Outline each blood parasite and name the species.
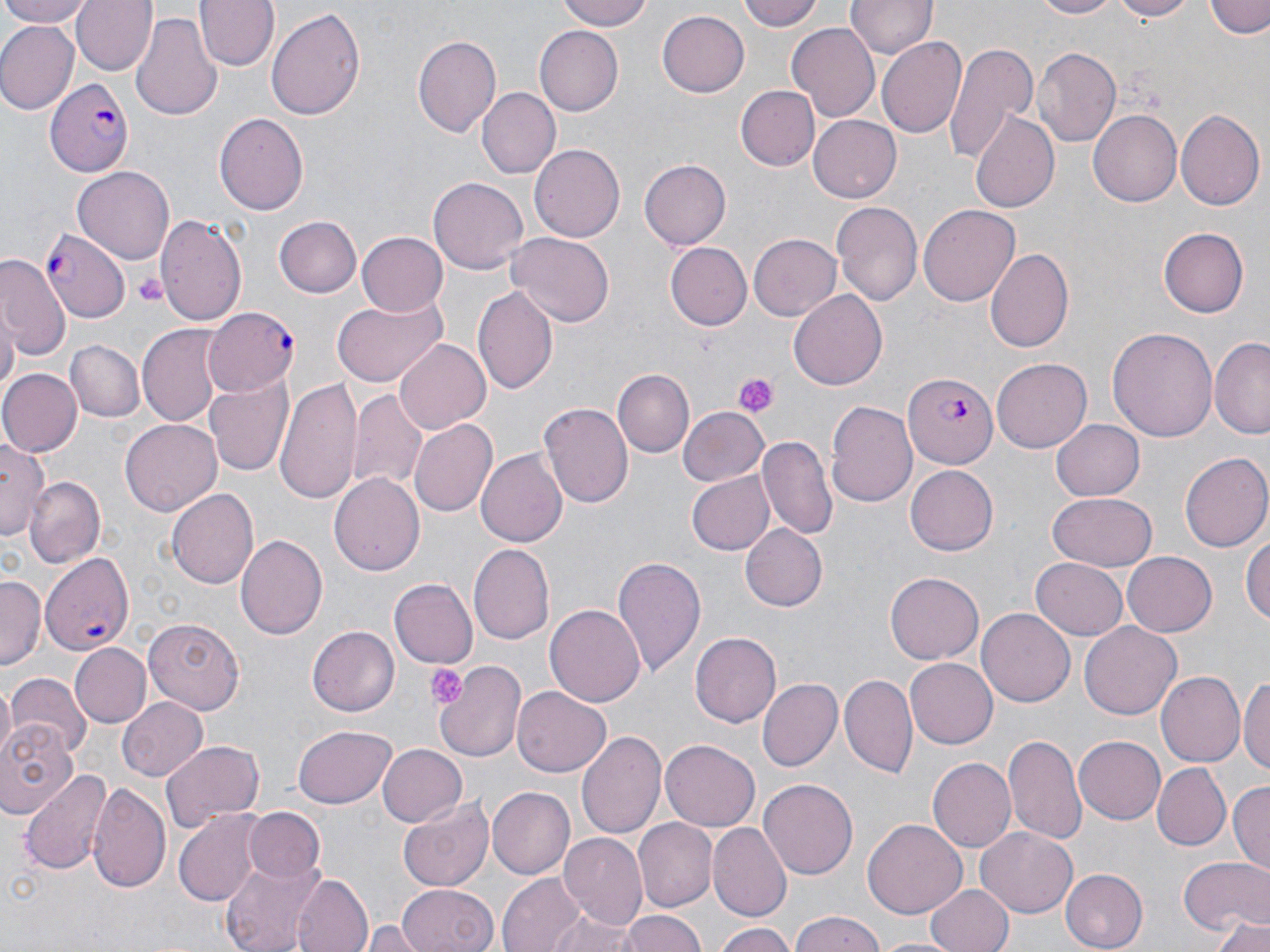
Approximate bounding boxes as (x1,y1)-(x2,y2) corner pairs in pixels.
Plasmodium falciparum-infected red blood cells: (46,79)-(132,176), (41,229)-(130,323), (201,308)-(299,393), (904,370)-(998,470), (41,551)-(133,655).
No Plasmodium ovale, Plasmodium malariae, Plasmodium vivax, Babesia divergens, or Trypanosoma brucei observed.

slide-level diagnosis = Plasmodium falciparum
modality = light microscopy
stain = May-Grünwald-Giemsa
magnification = 1000x
uninfected red blood cell locations = approximate bounding boxes as (x1,y1)-(x2,y2) corner pairs in pixels: (0,0)-(93,27), (72,0)-(158,76), (197,0)-(278,72), (554,0)-(655,31), (742,0)-(826,32), (1025,0)-(1123,19), (1107,0)-(1196,20), (1208,0)-(1270,39), (845,1)-(935,60), (266,6)-(367,122), (657,10)-(749,97), (132,11)-(220,120), (787,23)-(881,123), (0,24)-(78,112), (533,26)-(623,116), (413,34)-(501,139), (878,37)-(967,139), (942,44)-(1037,162), (1033,47)-(1121,146), (736,86)-(820,171), (478,88)-(559,178), (1088,110)-(1181,207), (1176,110)-(1264,211), (215,112)-(309,215), (970,112)-(1062,212), (807,114)-(901,204), (529,142)-(626,242), (640,159)-(731,249), (73,166)-(177,263), (429,177)-(529,274), (832,201)-(923,305), (919,205)-(1021,306), (155,211)-(247,326), (275,217)-(363,298), (1158,227)-(1250,317), (358,231)-(450,316), (747,231)-(841,322), (508,233)-(612,327), (664,242)-(750,330), (983,248)-(1072,353), (0,256)-(69,359), (472,285)-(559,397), (788,290)-(888,392), (332,293)-(446,387), (0,307)-(18,401), (137,324)-(226,429), (1107,326)-(1217,441), (1211,337)-(1270,438), (394,339)-(489,433), (63,340)-(144,422), (992,358)-(1092,453), (0,369)-(80,457), (614,369)-(694,456), (204,375)-(294,479), (275,379)-(362,502), (349,390)-(430,493), (827,398)-(919,509), (540,400)-(634,509), (678,404)-(768,486), (409,418)-(497,519), (121,419)-(222,517), (1052,421)-(1144,500), (1,434)-(47,543), (758,435)-(834,538), (476,450)-(567,548), (1181,453)-(1270,554), (905,464)-(999,555), (328,472)-(425,574), (688,472)-(776,554), (25,476)-(106,568), (167,487)-(259,590), (1048,491)-(1156,569), (740,523)-(827,612), (1241,532)-(1270,629), (236,535)-(327,639), (469,543)-(555,643), (1120,552)-(1216,636), (611,556)-(705,675), (1028,557)-(1128,639), (885,573)-(983,664), (1,575)-(47,672), (390,577)-(478,668), (545,604)-(645,707), (978,608)-(1074,707), (142,619)-(244,714), (1081,623)-(1182,720), (307,626)-(399,715), (690,631)-(782,728), (71,644)-(149,725), (905,657)-(1000,748), (434,658)-(528,764), (1156,671)-(1244,768), (1240,673)-(1269,779), (4,674)-(93,757), (840,675)-(918,780), (756,678)-(842,772), (513,688)-(611,776), (118,696)-(210,781), (0,720)-(79,817), (294,725)-(396,808), (579,729)-(668,841), (1002,732)-(1085,844), (1074,734)-(1166,823), (661,739)-(759,830), (162,740)-(265,830), (376,744)-(466,828), (929,757)-(1016,853), (1153,762)-(1231,849), (20,767)-(114,877), (760,779)-(856,879), (89,780)-(170,892), (1228,781)-(1270,872), (487,787)-(575,879), (398,799)-(494,891), (172,808)-(263,907), (242,809)-(325,882), (632,819)-(717,912), (862,820)-(967,919), (711,822)-(790,920), (976,824)-(1077,915), (560,834)-(650,928), (219,857)-(324,950), (1179,857)-(1270,936), (1060,868)-(1147,951), (498,871)-(592,952), (293,874)-(374,952), (926,883)-(1014,952), (395,884)-(497,952), (542,905)-(642,952), (615,910)-(709,952), (789,910)-(885,952), (1215,914)-(1270,952), (716,921)-(796,952), (361,922)-(423,950), (872,935)-(963,952)
image size = 1270×952 pixels
preparation = thin blood smear
platelet locations = approximate bounding boxes as (x1,y1)-(x2,y2) corner pairs in pixels: (131,271)-(168,307), (734,373)-(776,416), (425,663)-(469,710)
field of view = one of a larger specimen